Assess this cell for malaria.
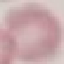
Uninfected.

Giemsa-stained preparation. Cell patch, automatically extracted from a larger field of view and resized to 64 × 64 pixels. Acquired by smartphone through the microscope eyepiece. Thin blood film.